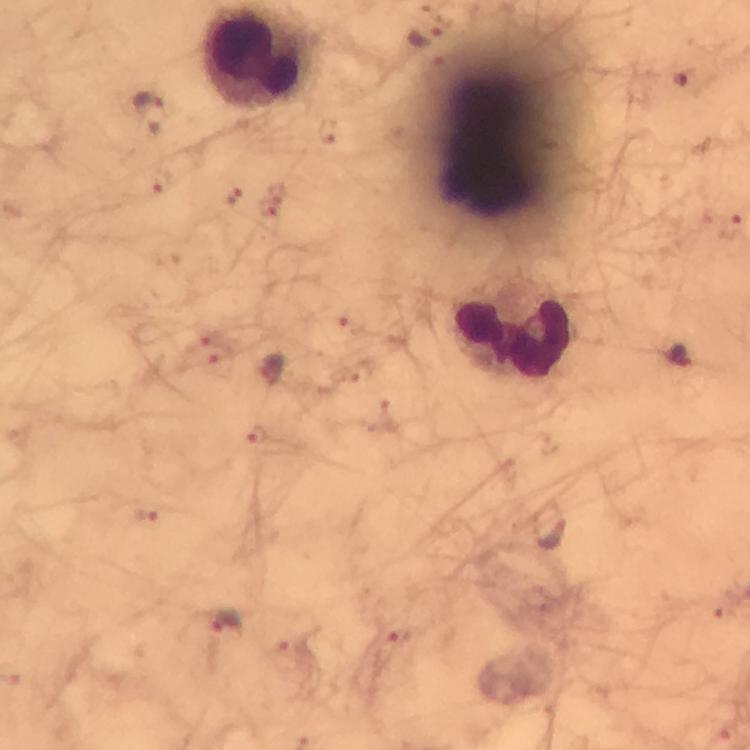
Approximate centers as [x, y] in pixels. Malaria parasite locations: [428, 34], [684, 78], [147, 98], [325, 131], [161, 180], [234, 197], [270, 205], [351, 322], [207, 351], [679, 356], [271, 370], [258, 437], [143, 515], [550, 527], [723, 607], [226, 622], [400, 636]. Leukocyte locations: [259, 58], [516, 335]. From a malaria diagnostic workup. A crop from one field of view. Image is 750×750 pixels. Thick smear. Photographed through the microscope with a smartphone camera. Giemsa stain. At 100x magnification. Immersion oil was used.